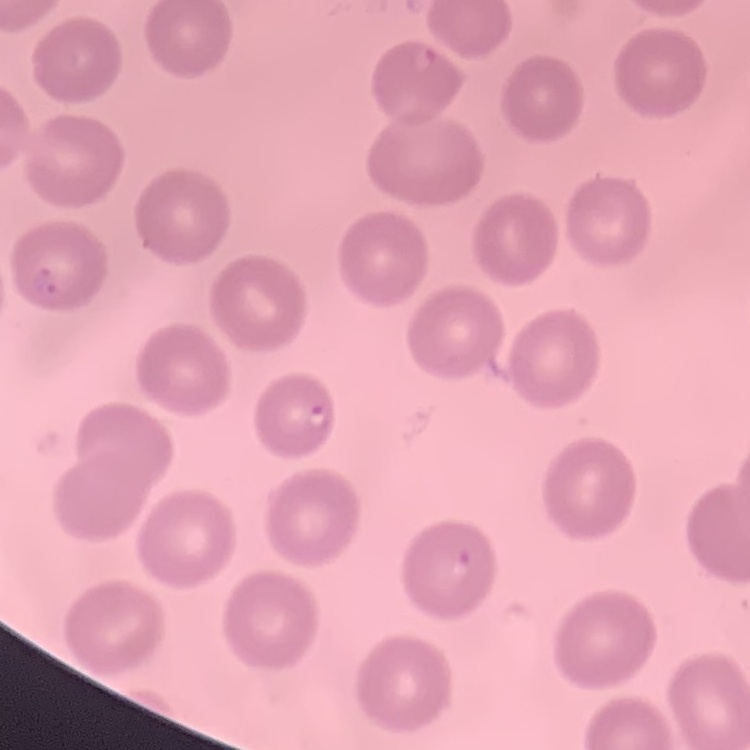

erythrocyte morphology = no rouleaux formation
stain = Field's or Giemsa
image type = square crop of a larger photomicrograph
preparation = thin peripheral smear